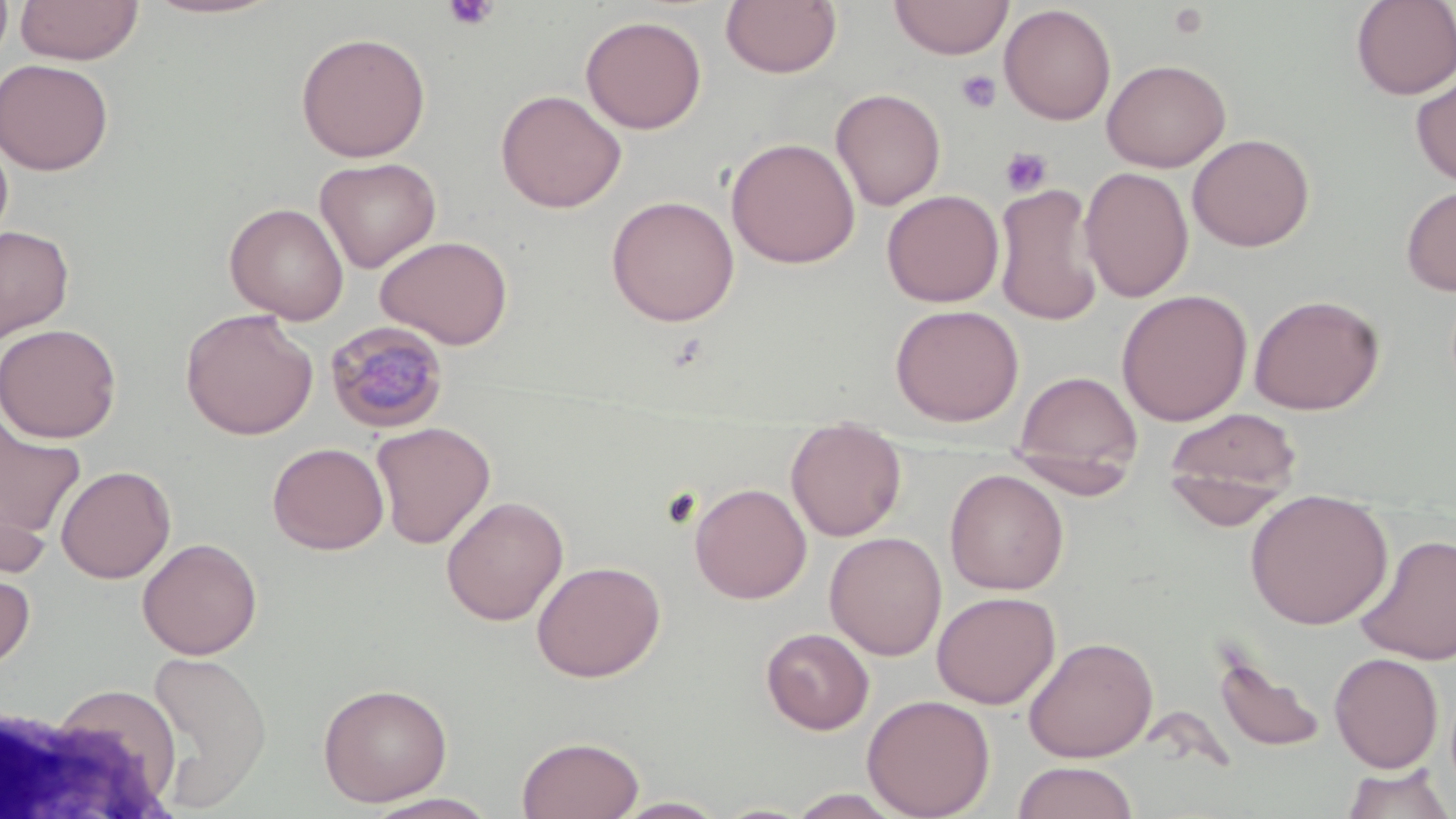 Approximate bounding boxes as (x1,y1)-(x2,y2) corner pairs in pixels. Plasmodium malariae-infected red blood cell locations: (324,320)-(449,434). Uninfected red blood cell locations: (14,0)-(144,65), (140,0)-(286,20), (720,0)-(842,79), (888,0)-(1014,60), (1350,0)-(1455,99), (999,4)-(1116,125), (580,14)-(707,134), (295,31)-(431,162), (0,58)-(114,175), (1101,58)-(1231,172), (1411,70)-(1456,188), (831,87)-(946,211), (494,89)-(627,213), (0,130)-(14,248), (1187,133)-(1315,252), (725,137)-(860,269), (314,156)-(441,273), (1079,166)-(1194,303), (994,184)-(1103,327), (1400,184)-(1456,296), (882,189)-(1004,307), (605,195)-(740,327), (224,202)-(349,324), (0,225)-(75,343), (375,235)-(513,349), (1116,289)-(1253,426), (1248,293)-(1385,416), (889,303)-(1024,427), (180,308)-(319,440), (0,323)-(122,443), (1013,370)-(1143,485), (1163,406)-(1303,524), (1,416)-(86,549), (371,421)-(496,549), (786,423)-(907,541), (267,441)-(389,555), (1005,447)-(1137,503), (55,465)-(176,583), (944,469)-(1069,595), (689,481)-(812,604), (1245,488)-(1393,629), (441,495)-(569,626), (824,531)-(947,660), (1354,532)-(1456,666), (137,537)-(262,660), (531,560)-(666,682), (0,562)-(36,673), (931,591)-(1061,709), (760,627)-(874,734), (1023,636)-(1159,762), (1212,647)-(1328,755), (143,649)-(273,810), (1329,652)-(1444,773), (317,682)-(453,807), (29,683)-(185,814), (861,694)-(996,818), (516,735)-(644,818), (1012,761)-(1139,819), (1339,764)-(1454,819), (785,789)-(906,818), (361,792)-(501,818), (610,796)-(730,818). Platelet locations: (443,0)-(500,32), (1167,3)-(1211,40), (956,70)-(1002,113), (1000,147)-(1053,197). Slide-level diagnosis: Plasmodium malariae. Optical microscopy. Captured at 1000x magnification. One field of a larger specimen. Thin blood film. Image is 1456×819 pixels. May-Grünwald-Giemsa stain.